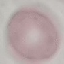

result: negative for malaria parasites
image_type: cell patch, automatically extracted from a larger field of view and resized to 64 × 64 pixels
capture: smartphone camera at the microscope eyepiece
preparation: thin smear
stain: Giemsa